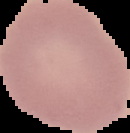 From a thin blood film. Image is 130×133 pixels. Malaria status: uninfected. Segmented cell region on a black background.